Identify the cell.
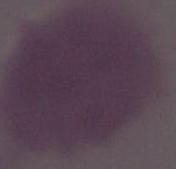
An erythrocyte.

modality: photomicrograph
magnification: 1000x